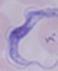

Summary:
  - Identification: trypanosome
  - Magnification: 1000x
  - Modality: photomicrograph